Identify the preparation type.
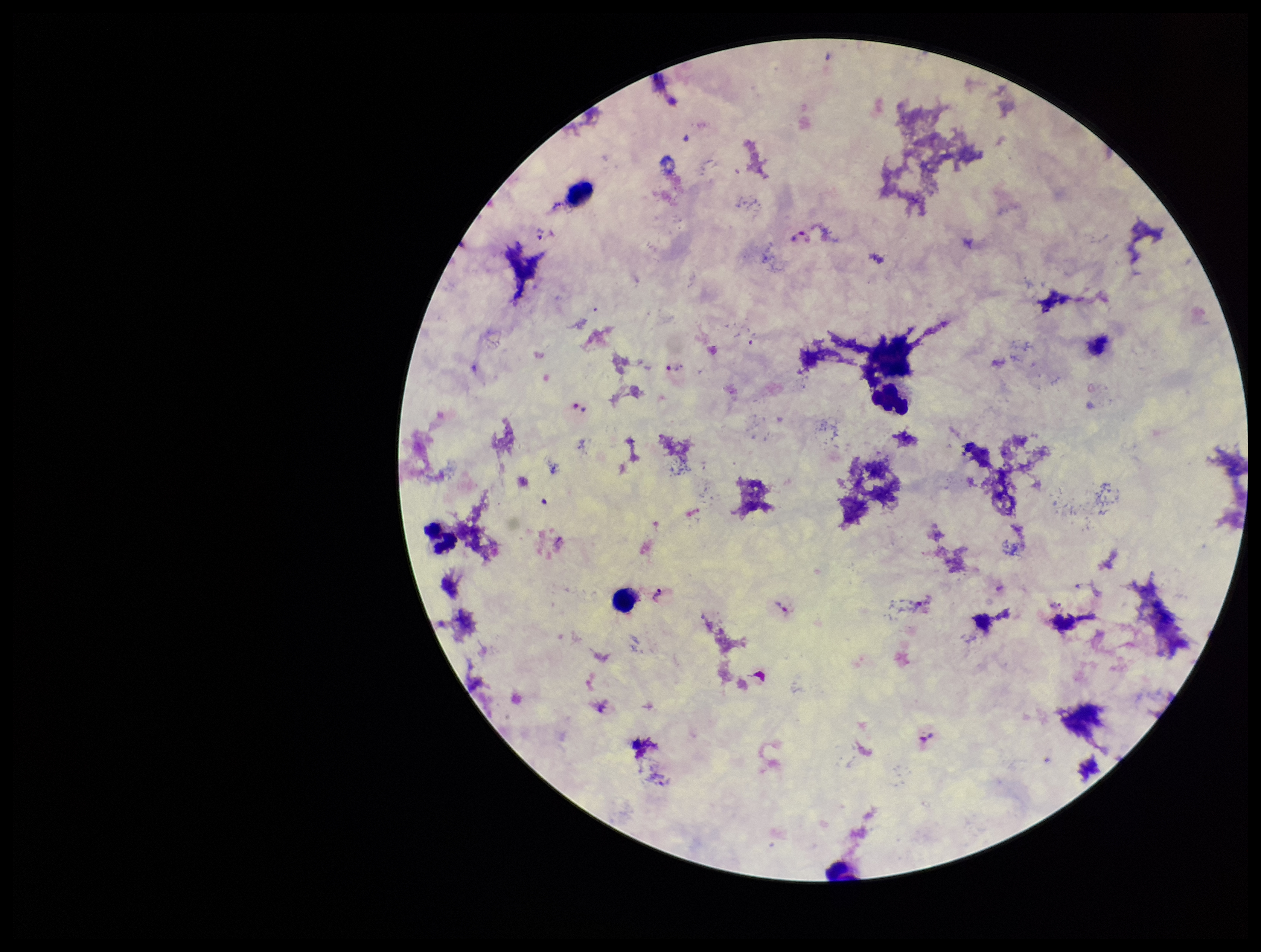

A thick smear.

One field from this slide. Species reported for this patient: Plasmodium vivax. Plasmodium parasites: identified. Smartphone photograph taken through the eyepiece of a microscope. Stained with Giemsa. Patient malaria status: infected. Parasite count: 7. Leukocyte count: 6. Image is 1261×952 pixels.